Locate and identify every blood parasite.
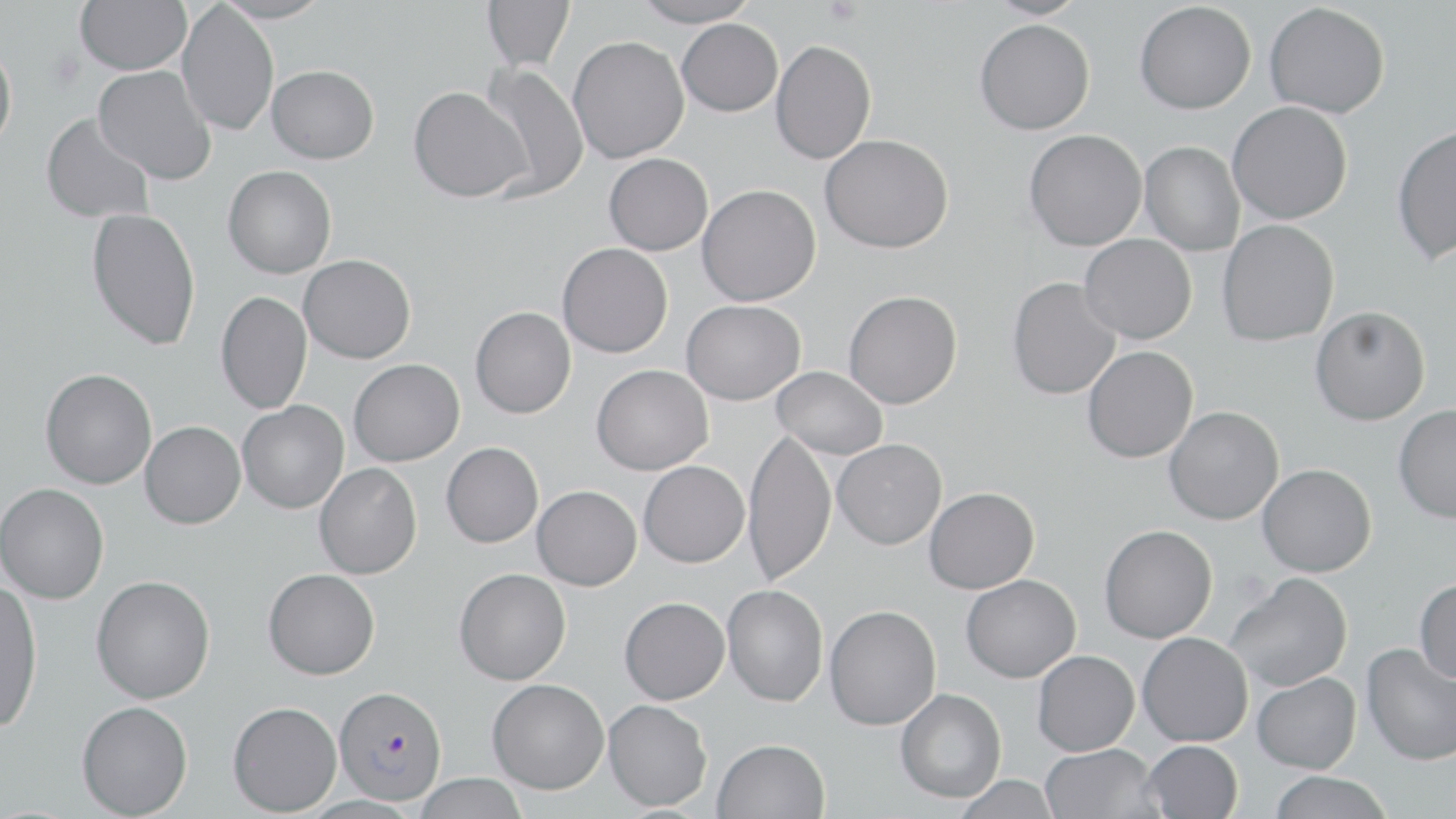
Approximate bounding boxes as (x1,y1)-(x2,y2) corner pairs in pixels.
Plasmodium falciparum-infected red blood cells: (334,685)-(447,805).
No Plasmodium ovale, Plasmodium malariae, Plasmodium vivax, Babesia divergens, or Trypanosoma brucei observed.

Platelet locations: (823,0)-(862,25). Uninfected red blood cell locations: (75,0)-(191,75), (215,0)-(332,24), (482,0)-(575,71), (629,0)-(760,27), (983,0)-(1090,20), (1134,1)-(1256,114), (176,2)-(279,136), (1264,2)-(1390,118), (677,18)-(783,116), (974,19)-(1095,135), (568,36)-(689,163), (770,39)-(877,164), (0,42)-(17,153), (478,62)-(589,200), (93,65)-(217,185), (266,65)-(379,164), (408,86)-(531,203), (1227,101)-(1353,224), (41,113)-(155,224), (1391,124)-(1456,265), (1024,129)-(1147,251), (820,134)-(954,254), (1139,141)-(1245,256), (603,153)-(713,255), (223,166)-(336,278), (697,184)-(821,306), (86,207)-(201,351), (1217,219)-(1339,346), (1079,234)-(1197,344), (557,243)-(673,358), (299,254)-(416,364), (1007,277)-(1121,400), (215,290)-(312,414), (844,290)-(963,408), (681,299)-(805,405), (470,306)-(576,418), (1310,306)-(1430,425), (1082,346)-(1198,463), (348,358)-(464,466), (591,364)-(713,475), (772,366)-(888,459), (40,368)-(157,489), (237,400)-(349,514), (1393,405)-(1456,523), (1164,406)-(1284,525), (140,421)-(245,529), (743,427)-(836,587), (832,438)-(947,550), (441,442)-(543,548), (638,460)-(749,567), (314,463)-(422,580), (1258,464)-(1377,577), (0,483)-(109,604), (532,485)-(642,590), (924,486)-(1040,593), (1099,524)-(1217,643), (263,568)-(380,680), (454,568)-(571,685), (1225,572)-(1352,691), (960,574)-(1081,682), (91,575)-(215,704), (1414,579)-(1456,683), (0,581)-(43,734), (722,584)-(828,707), (619,596)-(729,704), (824,604)-(941,730), (1137,632)-(1253,746), (1361,643)-(1455,765), (1032,650)-(1139,756), (1252,671)-(1361,773), (487,678)-(609,794), (896,688)-(1007,802), (603,699)-(712,811), (76,701)-(193,818), (228,701)-(342,816), (713,738)-(830,819), (1141,740)-(1243,818), (1040,744)-(1161,819), (1268,772)-(1392,818), (412,773)-(529,819), (953,774)-(1061,819). Slide-level diagnosis: Plasmodium falciparum. Captured at 1000x magnification. Thin blood film. Light microscopy. May-Grünwald-Giemsa-stained preparation. Image is 1456×819 pixels. Single field of view.